Outline each uninfected red blood cell.
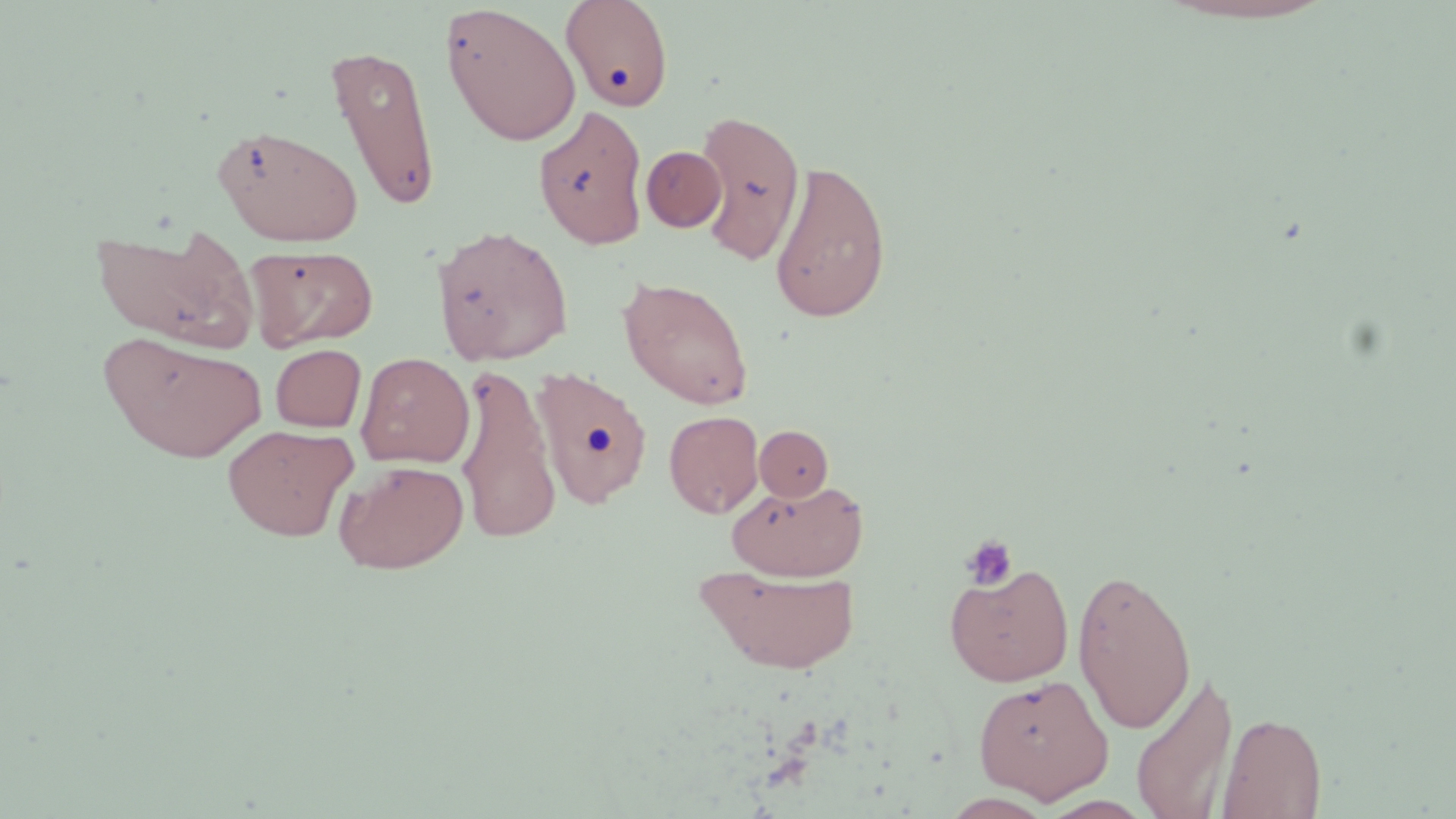

Approximate bounding boxes as [x1, y1, x2, y2] in pixels.
Uninfected red blood cells: [561, 0, 674, 113], [440, 3, 581, 147], [326, 44, 441, 212], [533, 104, 649, 249], [695, 109, 806, 264], [212, 123, 364, 247], [641, 145, 727, 232], [769, 159, 892, 323], [91, 221, 260, 353], [431, 224, 574, 365], [247, 244, 378, 351], [618, 276, 754, 410], [99, 332, 267, 463], [270, 344, 366, 432], [356, 352, 474, 468], [531, 363, 654, 510], [455, 364, 561, 545], [664, 410, 764, 518], [223, 424, 358, 541], [754, 425, 833, 502], [334, 460, 469, 573], [729, 480, 865, 581], [943, 560, 1075, 687], [696, 564, 862, 676], [1072, 566, 1196, 734], [1130, 667, 1239, 819], [973, 673, 1112, 802], [1217, 711, 1327, 819].

slide_level_diagnosis: no evidence of blood parasites
modality: optical microscopy
platelet_locations: 'approximate bounding boxes as [x1, y1, x2, y2] in pixels: [960, 534, 1019, 591]'
preparation: thin blood film
field_of_view: single
stain: May-Grünwald-Giemsa
image_size: 1456×819 pixels
magnification: 1000x